Locate every Plasmodium parasite.
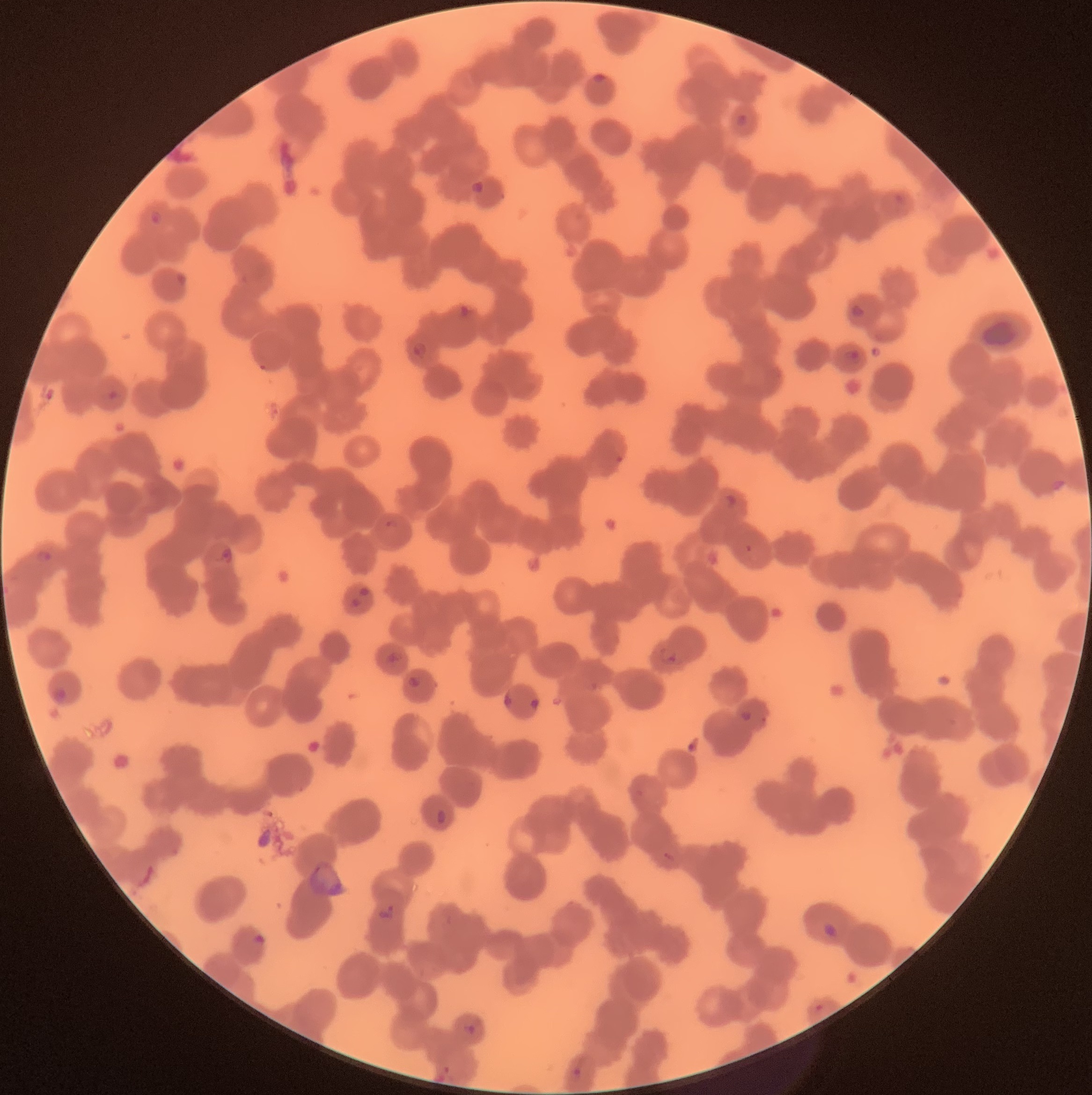

Approximate bounding boxes as (x1,y1)-(x2,y2) corner pairs in pixels.
Plasmodium parasites: (592,73)-(607,84), (736,114)-(748,128), (470,180)-(483,194), (149,209)-(164,226), (850,303)-(866,320), (458,304)-(477,320), (412,342)-(428,360), (845,349)-(860,363), (107,388)-(120,402), (725,493)-(738,509), (386,519)-(399,529), (219,546)-(233,563), (33,549)-(53,563), (357,587)-(370,598), (349,598)-(361,609), (659,647)-(681,665), (386,651)-(400,663), (407,676)-(422,690), (52,687)-(70,705), (503,693)-(513,708), (529,698)-(539,711), (740,709)-(753,722), (436,808)-(447,824), (378,903)-(395,922), (822,922)-(839,939), (252,932)-(268,946), (467,1024)-(475,1035), (571,1066)-(583,1080).

Light microscopy. The red blood cells show rouleaux formation. Image is 1092×1095 pixels. Thin blood film.